Outline each blood parasite and name the species.
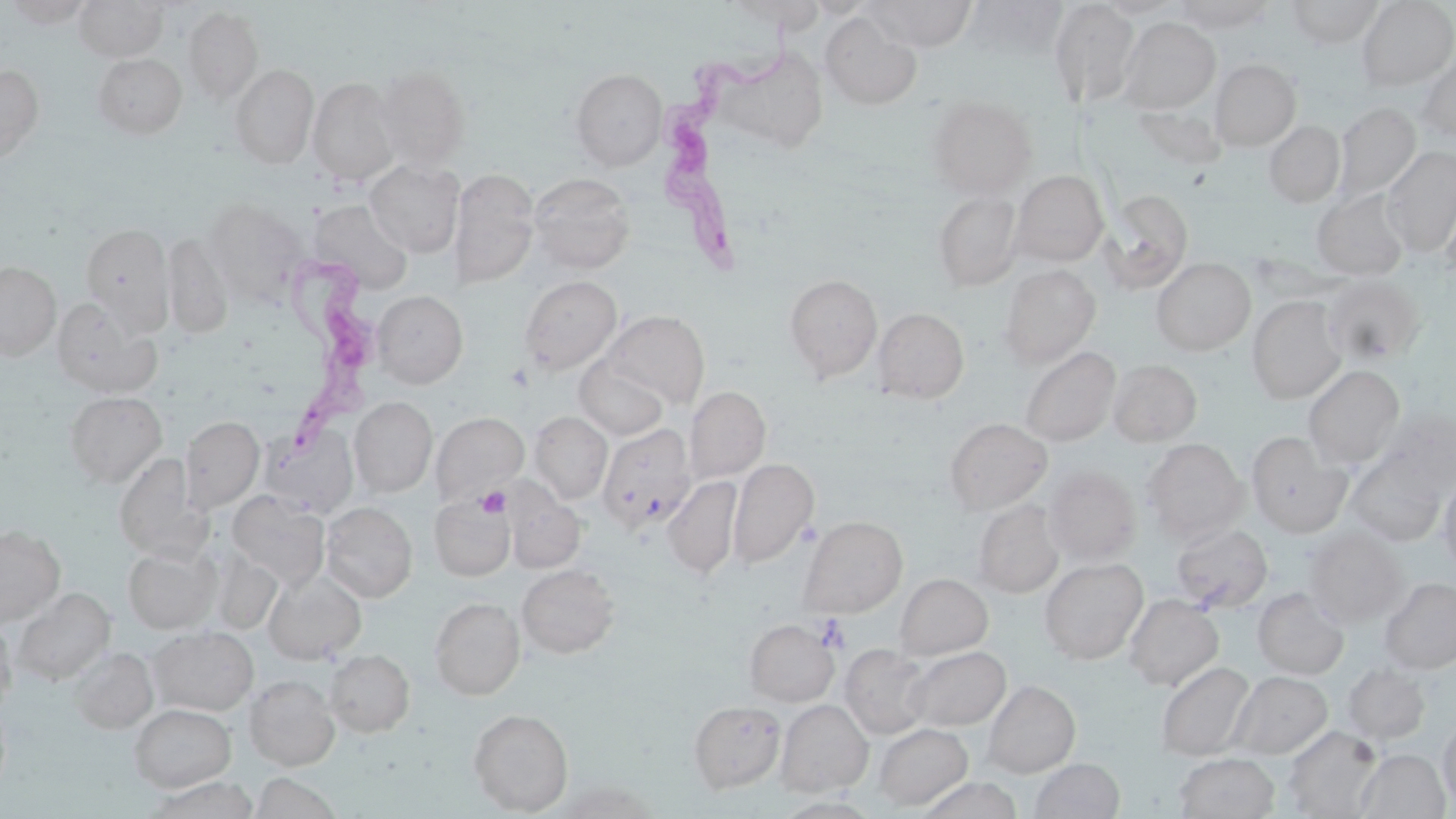

Approximate bounding boxes as (x1,y1)-(x2,y2) corner pairs in pixels.
Trypanosoma brucei: (654,10)-(800,278), (275,254)-(379,454).
No Plasmodium falciparum, Plasmodium ovale, Plasmodium malariae, Plasmodium vivax, or Babesia divergens observed.

slide-level diagnosis = Trypanosoma brucei
uninfected red blood cell locations = approximate bounding boxes as (x1,y1)-(x2,y2) corner pairs in pixels: (4,0)-(94,27), (74,0)-(167,62), (866,0)-(977,51), (1048,0)-(1139,110), (1094,0)-(1185,19), (1287,0)-(1383,47), (1356,0)-(1456,90), (722,1)-(827,30), (1173,1)-(1274,33), (183,6)-(263,104), (820,13)-(922,110), (1118,17)-(1220,113), (725,50)-(833,148), (1417,51)-(1456,145), (92,53)-(187,138), (1210,59)-(1300,151), (230,64)-(318,167), (0,65)-(44,164), (374,65)-(470,170), (571,68)-(666,170), (308,77)-(399,184), (927,96)-(1036,198), (1334,102)-(1421,203), (1133,103)-(1225,170), (1264,120)-(1345,208), (1381,146)-(1456,256), (365,159)-(464,257), (450,168)-(539,288), (1012,171)-(1108,265), (528,172)-(636,273), (1099,189)-(1194,293), (1313,189)-(1409,280), (933,191)-(1022,290), (203,199)-(304,305), (310,201)-(413,292), (80,223)-(175,334), (162,233)-(234,338), (1152,258)-(1256,355), (0,262)-(60,359), (999,265)-(1100,367), (784,273)-(882,382), (519,275)-(622,375), (1322,275)-(1424,367), (373,291)-(468,388), (1247,296)-(1345,403), (52,299)-(162,398), (872,307)-(969,404), (602,310)-(709,408), (1019,347)-(1120,446), (574,357)-(669,440), (1108,359)-(1202,446), (1303,366)-(1405,468), (684,386)-(770,483), (65,391)-(167,487), (350,396)-(437,497), (1377,409)-(1456,494), (530,411)-(612,503), (431,412)-(528,505), (181,416)-(264,511), (945,418)-(1053,514), (597,424)-(695,534), (259,425)-(358,518), (1246,433)-(1350,536), (1142,439)-(1248,543), (113,453)-(205,558), (1346,455)-(1446,546), (728,458)-(818,567), (1044,466)-(1141,566), (1438,473)-(1456,574), (663,476)-(742,579), (227,491)-(330,591), (430,494)-(515,580), (508,494)-(585,572), (973,500)-(1063,598), (321,502)-(417,602), (798,516)-(908,617), (1171,523)-(1273,613), (0,525)-(65,625), (1304,527)-(1408,626), (123,544)-(221,633), (1039,557)-(1148,664), (517,564)-(619,658), (263,571)-(366,664), (896,573)-(993,659), (1380,577)-(1456,673), (1252,587)-(1349,679), (13,588)-(115,684), (1124,594)-(1223,691), (429,597)-(525,699), (0,618)-(17,712), (745,619)-(838,705), (149,627)-(258,715), (840,644)-(932,738), (70,646)-(158,733), (904,646)-(1010,731), (325,650)-(415,736), (1156,661)-(1255,761), (1343,663)-(1430,744), (1228,670)-(1331,759), (244,675)-(340,770), (982,680)-(1080,777), (689,700)-(785,793), (777,700)-(873,796), (129,703)-(236,792), (468,708)-(574,815), (1438,718)-(1456,809), (874,722)-(972,809), (1283,725)-(1383,817), (1355,748)-(1450,818), (1173,753)-(1280,818), (1029,758)-(1125,819), (250,772)-(342,818), (145,777)-(259,818)
modality = light microscopy
magnification = 1000x
platelet locations = approximate bounding boxes as (x1,y1)-(x2,y2) corner pairs in pixels: (475,486)-(510,518), (816,615)-(851,654)
image size = 1456×819 pixels
stain = May-Grünwald-Giemsa
field of view = one of a larger specimen
preparation = thin blood film